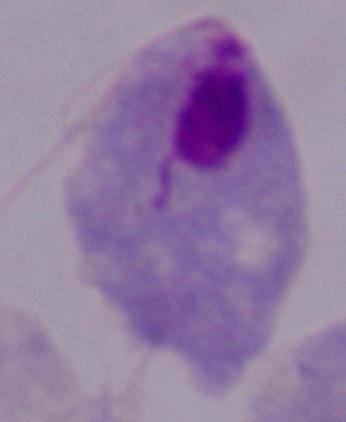

Summary:
  - Magnification: 1000x
  - Modality: photomicrograph
  - Identification: trichomonad